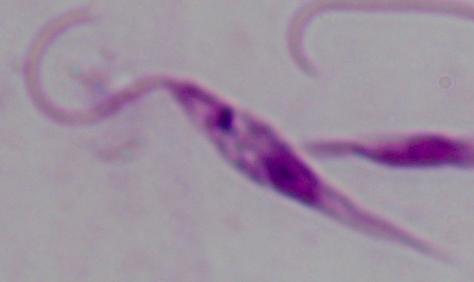
Summary:
  - Magnification: 1000x
  - Modality: micrograph
  - Identification: Leishmania